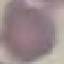
result = negative for malaria parasites
image type = automatically extracted cell patch, resized to 64 × 64 pixels
preparation = thin blood smear
capture = smartphone through the microscope eyepiece
stain = Giemsa